Give the extent of all uninfected red blood cells.
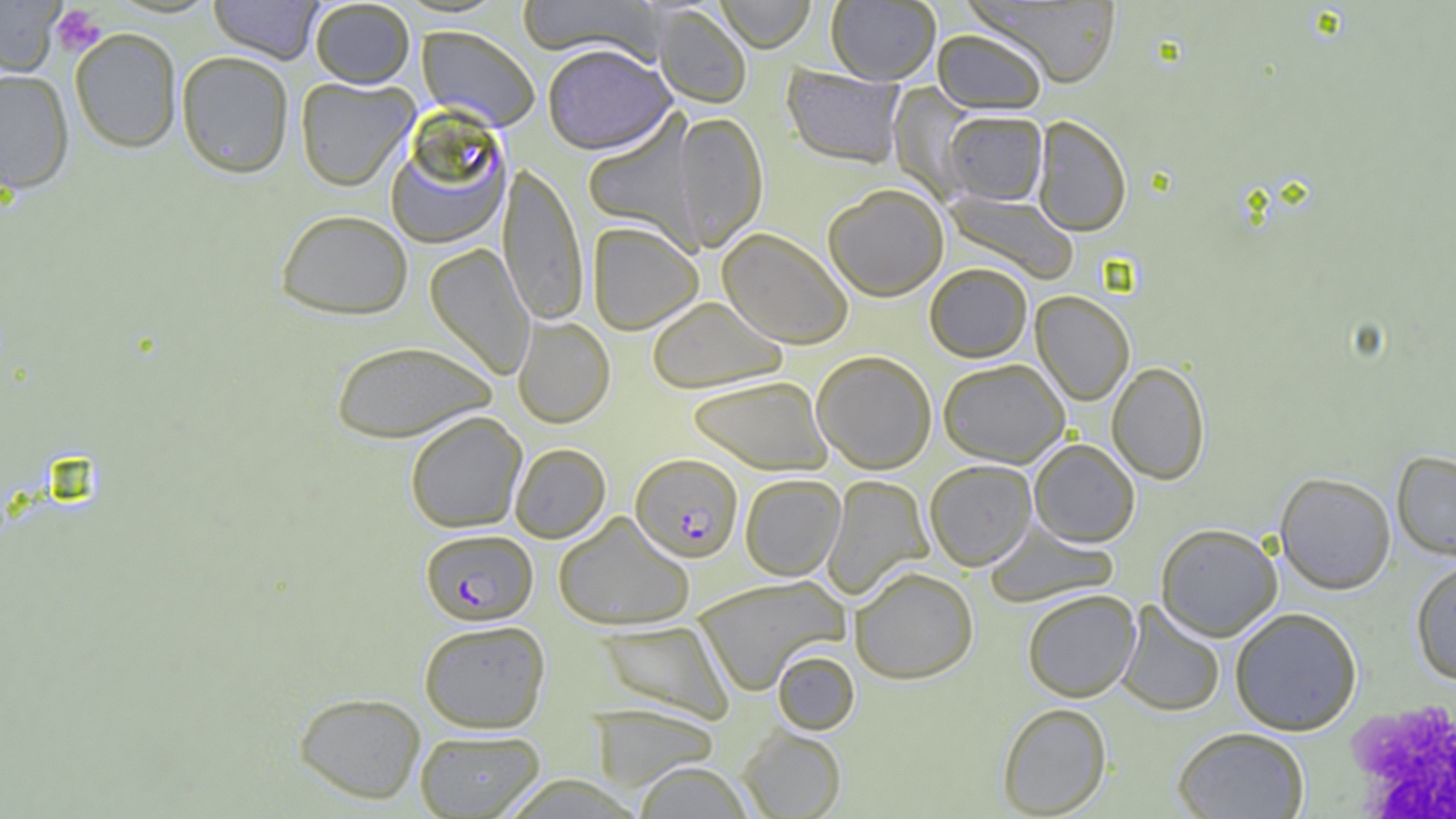

Approximate bounding boxes as (x1,y1)-(x2,y2) corner pairs in pixels.
Uninfected red blood cells: (0,0)-(64,75), (209,0)-(323,64), (310,0)-(415,88), (516,0)-(665,61), (715,0)-(817,53), (969,0)-(1122,88), (826,1)-(941,85), (652,6)-(751,109), (417,25)-(541,131), (70,27)-(183,153), (931,28)-(1048,114), (71,39)-(294,160), (543,43)-(675,155), (176,50)-(294,178), (782,65)-(906,169), (0,69)-(74,194), (295,76)-(418,191), (888,82)-(981,203), (942,110)-(1047,206), (582,112)-(704,252), (673,112)-(768,251), (1032,115)-(1131,236), (383,116)-(513,249), (498,161)-(589,326), (823,184)-(949,301), (944,190)-(1079,284), (275,209)-(413,320), (587,221)-(703,335), (717,227)-(854,349), (425,243)-(535,380), (925,262)-(1032,362), (1031,291)-(1134,405), (647,296)-(788,394), (513,316)-(615,428), (331,339)-(497,443), (812,350)-(937,474), (938,358)-(1069,467), (1107,361)-(1210,484), (688,375)-(832,475), (405,411)-(527,532), (1029,438)-(1139,547), (510,443)-(611,543), (1392,450)-(1456,560), (925,459)-(1037,570), (1275,471)-(1396,594), (740,473)-(845,581), (822,475)-(933,600), (553,511)-(694,630), (983,522)-(1118,607), (1155,522)-(1283,641), (1410,558)-(1456,684), (849,566)-(979,684), (693,575)-(849,694), (1022,589)-(1140,702), (1116,601)-(1225,716), (1229,607)-(1361,735), (418,619)-(551,733), (597,619)-(734,723), (772,649)-(860,735), (293,691)-(426,804), (997,702)-(1111,818), (589,703)-(721,792), (737,725)-(846,819), (1172,726)-(1309,819), (415,729)-(545,817), (634,761)-(752,818).

Summary:
  - Plasmodium falciparum-infected red blood cell locations: (630,453)-(743,562), (420,528)-(538,626)
  - Platelet locations: (50,6)-(107,57), (1345,699)-(1456,817)
  - Slide-level diagnosis: Plasmodium falciparum
  - Field of view: single
  - Image size: 1456×819 pixels
  - Modality: light microscopy
  - Magnification: 1000x
  - Preparation: thin blood film